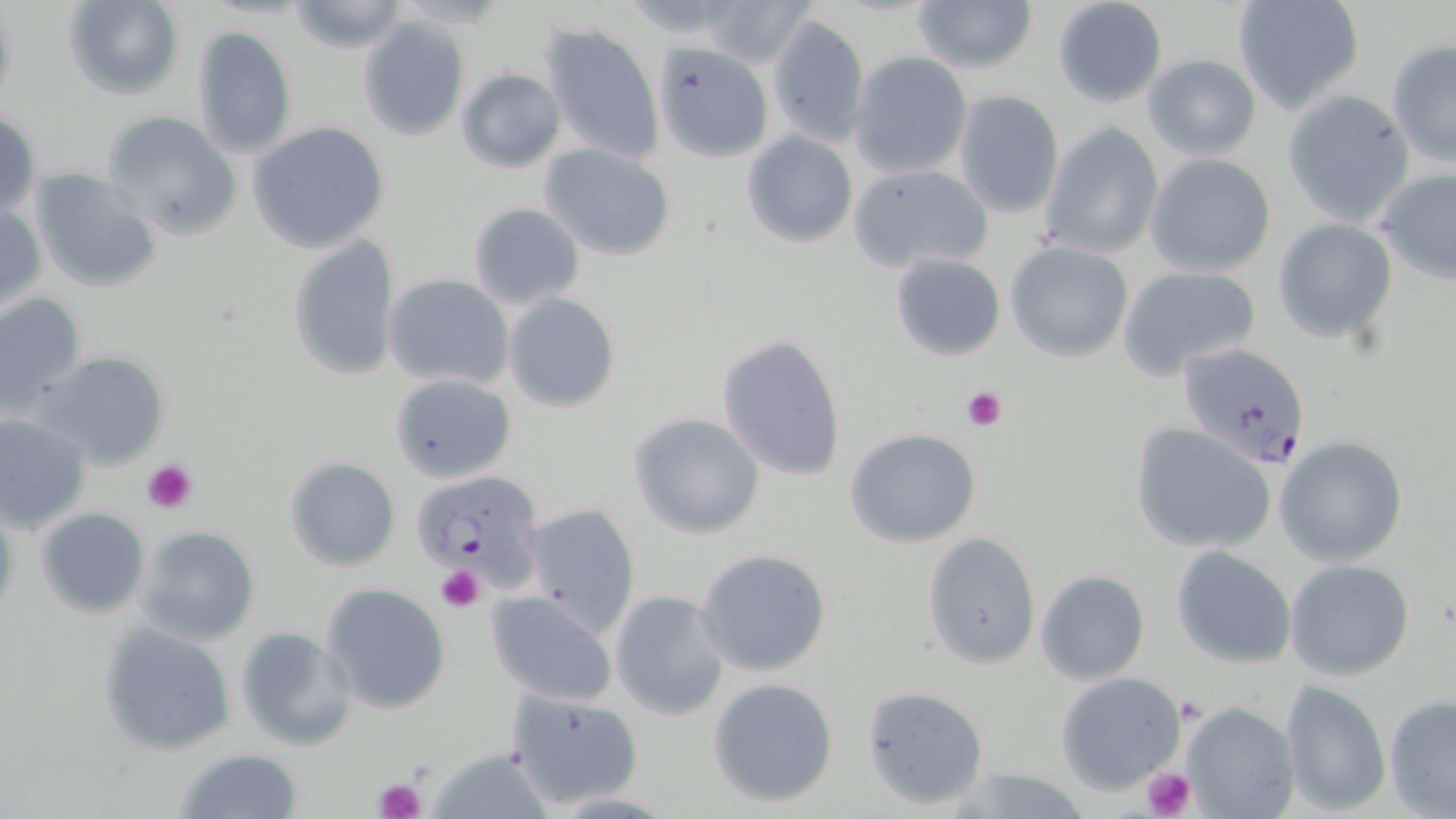
Summary:
  - Coordinate format: approximate bounding boxes as [x1, y1, x2, y2] in pixels
  - Plasmodium falciparum-infected red blood cell locations: [1178, 342, 1312, 467], [413, 468, 546, 592]
  - Uninfected red blood cell locations: [62, 0, 183, 101], [285, 0, 408, 52], [911, 0, 1038, 76], [1051, 0, 1169, 108], [1232, 0, 1364, 113], [696, 1, 813, 66], [768, 13, 869, 146], [358, 15, 469, 140], [541, 22, 664, 165], [190, 26, 298, 158], [1386, 40, 1456, 168], [654, 44, 773, 162], [849, 52, 973, 177], [1142, 54, 1262, 161], [456, 68, 565, 172], [871, 79, 1009, 204], [1282, 90, 1417, 227], [952, 91, 1065, 219], [101, 110, 241, 239], [1, 112, 41, 219], [248, 122, 390, 253], [1039, 122, 1164, 258], [741, 129, 857, 248], [540, 143, 676, 261], [1143, 153, 1278, 278], [850, 164, 993, 272], [30, 168, 162, 292], [1374, 168, 1456, 284], [0, 200, 45, 315], [467, 203, 584, 310], [1273, 218, 1399, 341], [288, 234, 401, 381], [1004, 240, 1134, 362], [889, 252, 1006, 362], [1118, 265, 1262, 378], [384, 274, 513, 389], [0, 292, 87, 416], [503, 293, 621, 413], [717, 333, 847, 482], [35, 351, 170, 468], [391, 373, 515, 482], [0, 411, 92, 533], [627, 412, 767, 538], [1130, 422, 1277, 553], [846, 427, 983, 547], [1274, 437, 1408, 568], [285, 458, 400, 571], [522, 502, 642, 637], [35, 507, 151, 618], [134, 527, 261, 646], [921, 532, 1041, 668], [1171, 546, 1297, 668], [694, 548, 832, 677], [1285, 559, 1416, 682], [1035, 569, 1151, 685], [322, 582, 451, 716], [610, 589, 730, 720], [486, 591, 619, 705], [98, 622, 237, 755], [235, 626, 358, 751], [1055, 672, 1185, 793], [707, 676, 839, 807], [1280, 680, 1392, 814], [863, 686, 989, 810], [506, 690, 641, 807], [1383, 693, 1456, 818], [1178, 700, 1300, 819], [173, 746, 304, 819], [428, 747, 554, 819], [944, 765, 1099, 819]
  - Platelet locations: [963, 385, 1005, 430], [144, 460, 197, 514], [437, 566, 485, 611], [1141, 765, 1196, 819], [371, 776, 425, 819]
  - Slide-level diagnosis: Plasmodium falciparum
  - Magnification: 1000x
  - Field of view: one of a larger specimen
  - Modality: optical microscopy
  - Preparation: thin blood smear
  - Image size: 1456×819 pixels
  - Stain: May-Grünwald-Giemsa